Classify this cell by malaria status.
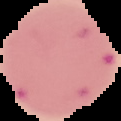
Parasitized.

Image is 121×121 pixels. Cell region segmented out of the field of view; the surrounding area is masked to black. From a thin blood film.